Give the position of every malaria parasite.
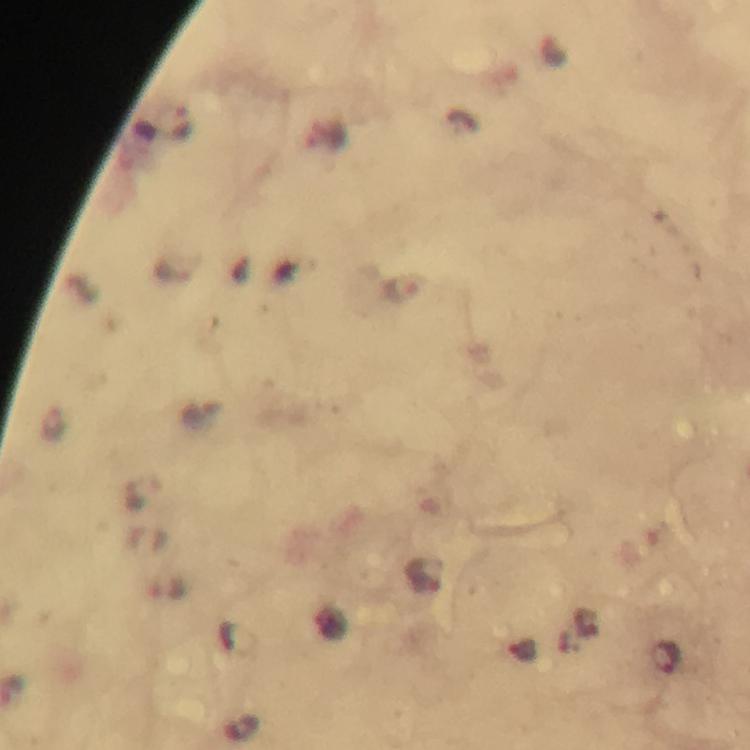
Approximate centers as {x, y} in pixels.
Malaria parasites: {406, 289}, {425, 575}, {522, 650}, {667, 660}.

{
  "immersion_oil": "used",
  "preparation": "thick blood smear",
  "cropped_from": "a single field of view",
  "capture": "smartphone photograph through a microscope",
  "stain": "Giemsa",
  "magnification": "100x",
  "context": "from a diagnostic examination for malaria",
  "image_size": "750×750 pixels"
}